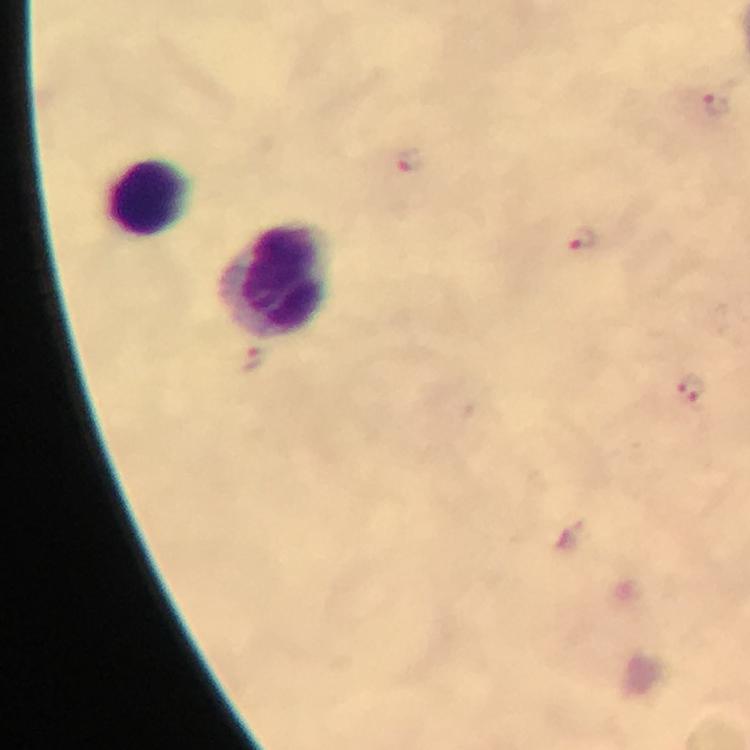

Approximate centers as {x, y} in pixels.
Summary:
  - Plasmodium parasite locations: {716, 104}, {409, 161}, {583, 239}, {251, 360}, {691, 389}
  - Leukocyte locations: {149, 197}, {275, 281}
  - Context: from a diagnostic examination for malaria
  - Cropped from: a single field of view
  - Capture: smartphone photograph through a microscope
  - Preparation: thick blood film
  - Image size: 750×750 pixels
  - Immersion oil: used
  - Magnification: 100x
  - Stain: Giemsa